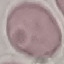
Result: no malaria parasites detected. Giemsa-stained preparation. Photographed with a smartphone camera at the microscope eyepiece. Cell patch, automatically extracted from a larger field of view and resized to 64 × 64 pixels. Thin smear of blood.